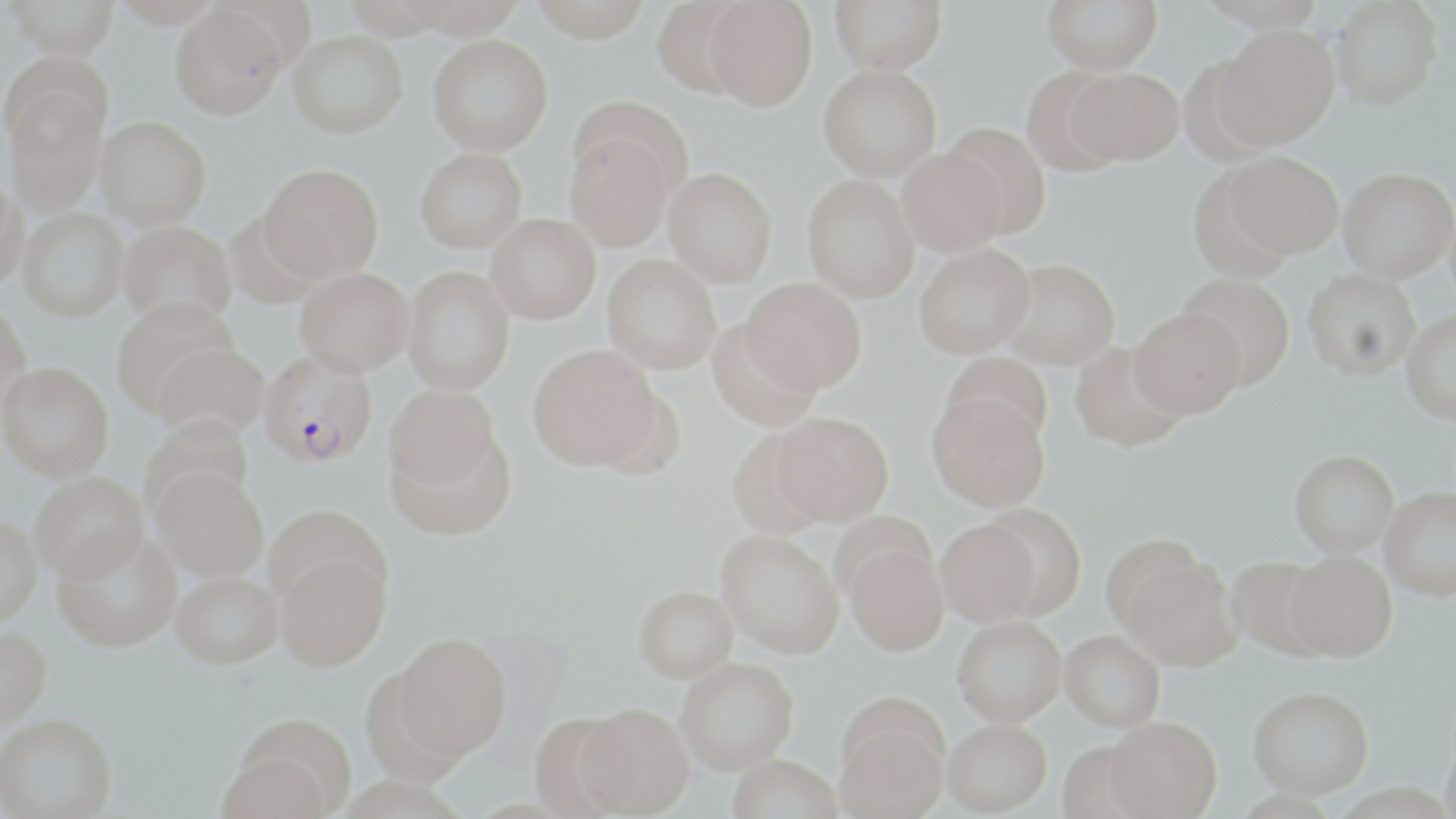

Plasmodium falciparum-infected red blood cell locations = approximate bounding boxes as named x1/y1/x2/y2 corners in pixels: (x1=258, y1=349, x2=378, y2=468)
slide-level diagnosis = Plasmodium falciparum
field of view = single
image size = 1456×819 pixels
magnification = 1000x
preparation = thin blood smear
stain = May-Grünwald-Giemsa
uninfected red blood cell locations = approximate bounding boxes as named x1/y1/x2/y2 corners in pixels: (x1=4, y1=0, x2=119, y2=59), (x1=110, y1=0, x2=225, y2=27), (x1=527, y1=0, x2=653, y2=42), (x1=651, y1=0, x2=754, y2=97), (x1=703, y1=0, x2=817, y2=111), (x1=829, y1=0, x2=946, y2=74), (x1=1042, y1=0, x2=1163, y2=75), (x1=1329, y1=0, x2=1443, y2=110), (x1=170, y1=5, x2=286, y2=119), (x1=1213, y1=24, x2=1340, y2=150), (x1=288, y1=30, x2=407, y2=138), (x1=428, y1=34, x2=553, y2=156), (x1=817, y1=64, x2=942, y2=181), (x1=1067, y1=67, x2=1184, y2=165), (x1=1019, y1=68, x2=1127, y2=176), (x1=4, y1=86, x2=107, y2=217), (x1=96, y1=116, x2=211, y2=230), (x1=941, y1=122, x2=1051, y2=240), (x1=564, y1=131, x2=674, y2=253), (x1=415, y1=146, x2=527, y2=252), (x1=897, y1=148, x2=1008, y2=256), (x1=1223, y1=151, x2=1344, y2=258), (x1=259, y1=162, x2=384, y2=282), (x1=1187, y1=165, x2=1297, y2=283), (x1=1338, y1=167, x2=1455, y2=282), (x1=664, y1=168, x2=777, y2=286), (x1=0, y1=174, x2=27, y2=291), (x1=802, y1=174, x2=919, y2=303), (x1=16, y1=208, x2=127, y2=322), (x1=225, y1=212, x2=328, y2=309), (x1=486, y1=214, x2=601, y2=324), (x1=119, y1=220, x2=236, y2=328), (x1=914, y1=242, x2=1036, y2=358), (x1=601, y1=254, x2=721, y2=374), (x1=997, y1=258, x2=1120, y2=369), (x1=401, y1=265, x2=514, y2=395), (x1=295, y1=266, x2=414, y2=376), (x1=1303, y1=269, x2=1421, y2=380), (x1=1178, y1=273, x2=1296, y2=390), (x1=741, y1=276, x2=867, y2=394), (x1=111, y1=297, x2=240, y2=418), (x1=0, y1=301, x2=32, y2=419), (x1=1129, y1=307, x2=1246, y2=419), (x1=1401, y1=310, x2=1456, y2=426), (x1=706, y1=319, x2=821, y2=432), (x1=154, y1=341, x2=269, y2=440), (x1=1069, y1=341, x2=1188, y2=453), (x1=528, y1=343, x2=662, y2=470), (x1=941, y1=351, x2=1053, y2=448), (x1=1, y1=361, x2=113, y2=481), (x1=384, y1=385, x2=501, y2=493), (x1=926, y1=392, x2=1050, y2=512), (x1=771, y1=411, x2=894, y2=526), (x1=140, y1=412, x2=255, y2=521), (x1=386, y1=423, x2=513, y2=539), (x1=1289, y1=449, x2=1399, y2=557), (x1=153, y1=467, x2=269, y2=581), (x1=29, y1=471, x2=149, y2=583), (x1=1380, y1=485, x2=1456, y2=600), (x1=981, y1=504, x2=1086, y2=619), (x1=263, y1=505, x2=387, y2=609), (x1=0, y1=513, x2=42, y2=627), (x1=935, y1=520, x2=1039, y2=628), (x1=716, y1=530, x2=844, y2=658), (x1=52, y1=532, x2=182, y2=652), (x1=843, y1=541, x2=950, y2=658), (x1=1286, y1=550, x2=1397, y2=661), (x1=276, y1=553, x2=390, y2=671), (x1=1117, y1=553, x2=1240, y2=672), (x1=1225, y1=556, x2=1334, y2=660), (x1=171, y1=571, x2=284, y2=669), (x1=633, y1=585, x2=738, y2=682), (x1=953, y1=617, x2=1067, y2=729), (x1=0, y1=624, x2=52, y2=731), (x1=391, y1=632, x2=511, y2=762), (x1=1059, y1=632, x2=1165, y2=733), (x1=676, y1=657, x2=798, y2=775), (x1=1249, y1=686, x2=1375, y2=799), (x1=575, y1=704, x2=694, y2=817), (x1=835, y1=707, x2=949, y2=819), (x1=526, y1=711, x2=635, y2=817), (x1=0, y1=712, x2=116, y2=817), (x1=1104, y1=720, x2=1222, y2=819), (x1=943, y1=723, x2=1052, y2=818), (x1=1440, y1=728, x2=1456, y2=819), (x1=217, y1=737, x2=343, y2=819), (x1=726, y1=756, x2=843, y2=819)
modality = optical microscopy